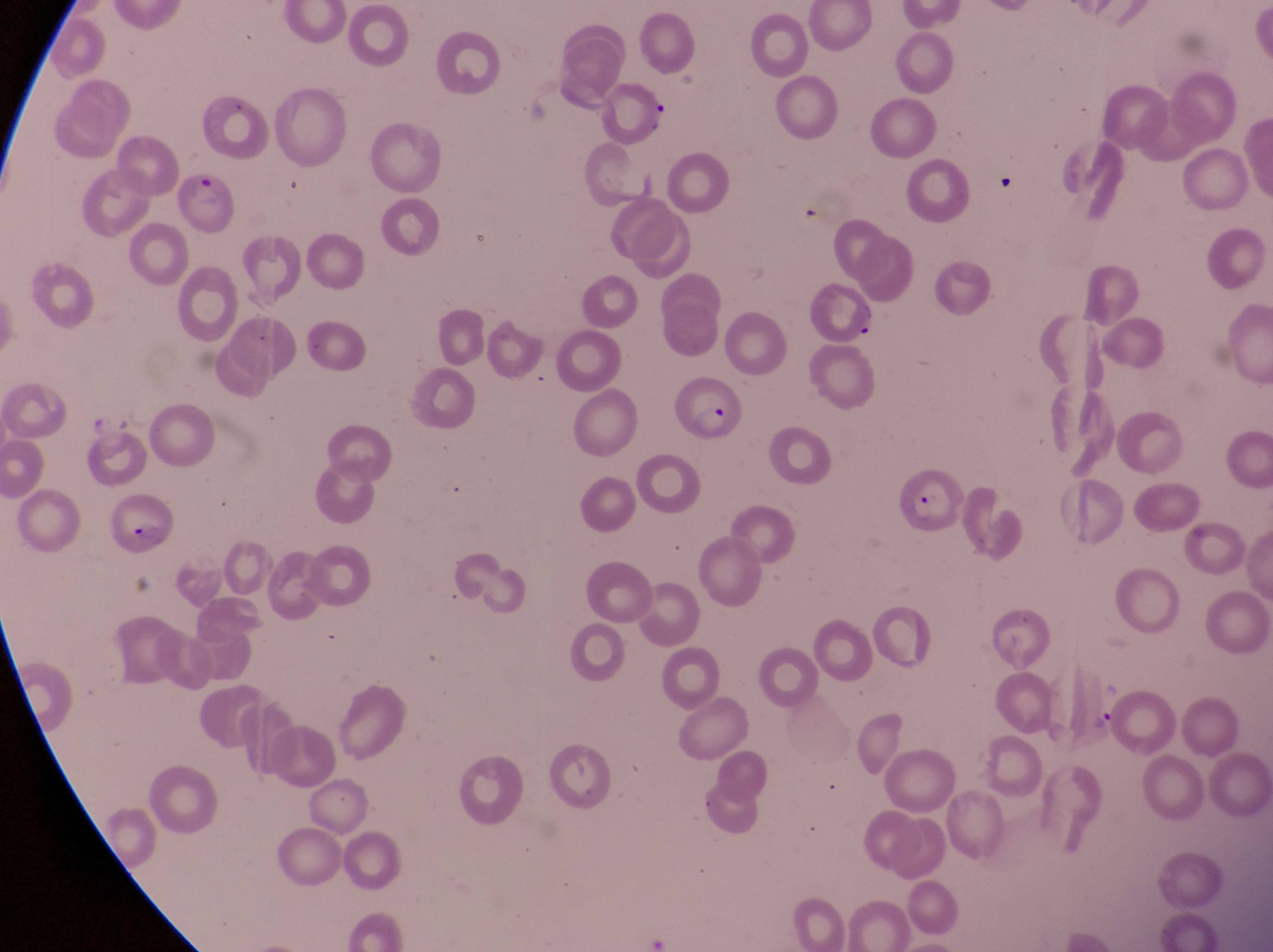
Approximate bounding boxes as (left, top, right, bottom) in pixels.
Summary:
  - Parasitised red blood cell locations: (172, 174, 235, 237), (672, 379, 749, 446), (893, 460, 962, 542), (99, 494, 176, 554)
  - Trophozoite locations: (1088, 702, 1120, 744)
  - Artifact (platelet-like body, stain precipitate, or debris) locations: (642, 102, 672, 134), (991, 174, 1018, 199)
  - Capture: smartphone photograph through the eyepiece of an Olympus CX-23 microscope
  - Image size: 1273×952 pixels
  - Country: Uganda
  - Magnification: 1000x
  - Preparation: thin blood film
  - Field of view: single